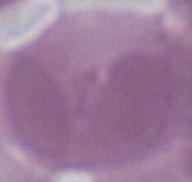
identification = red blood cell
magnification = 1000x
modality = photomicrograph